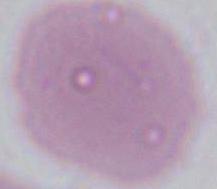

A red blood cell is seen. Photomicrograph. Captured at 1000x magnification.